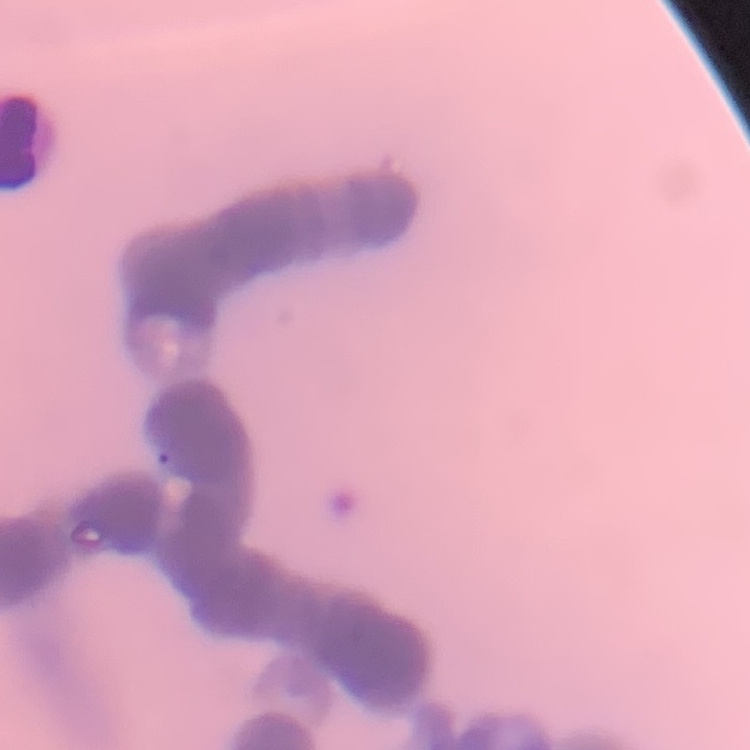
The red blood cells exhibit rouleaux formation. Field's or Giemsa stain. Thin peripheral smear. Square crop of a larger photomicrograph.